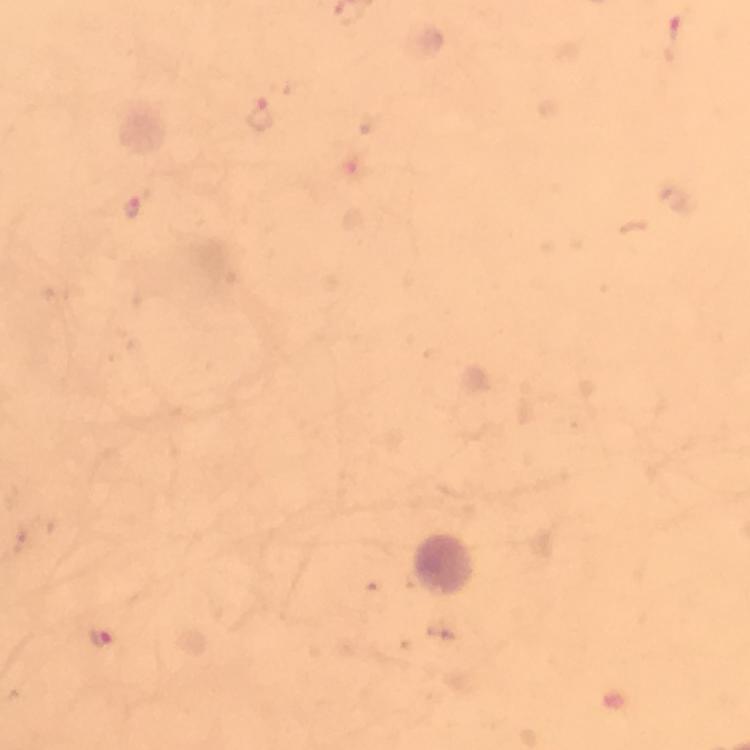

Approximate centers as [x, y] in pixels.
Summary:
  - Malaria parasite locations: [674, 41], [263, 114], [132, 206], [101, 638]
  - Stain: Giemsa
  - Cropped from: a single field of view
  - Preparation: thick smear
  - Context: from a malaria diagnostic workup
  - Image size: 750×750 pixels
  - Capture: smartphone mounted on the microscope
  - Magnification: 100x
  - Immersion oil: used